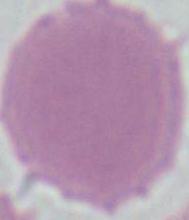
Summary:
  - Modality: photomicrograph
  - Magnification: 1000x
  - Identification: red blood cell